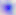
Summary:
  - Magnification: 400x
  - Identification: Toxoplasma gondii
  - Modality: photomicrograph